Outline platelets.
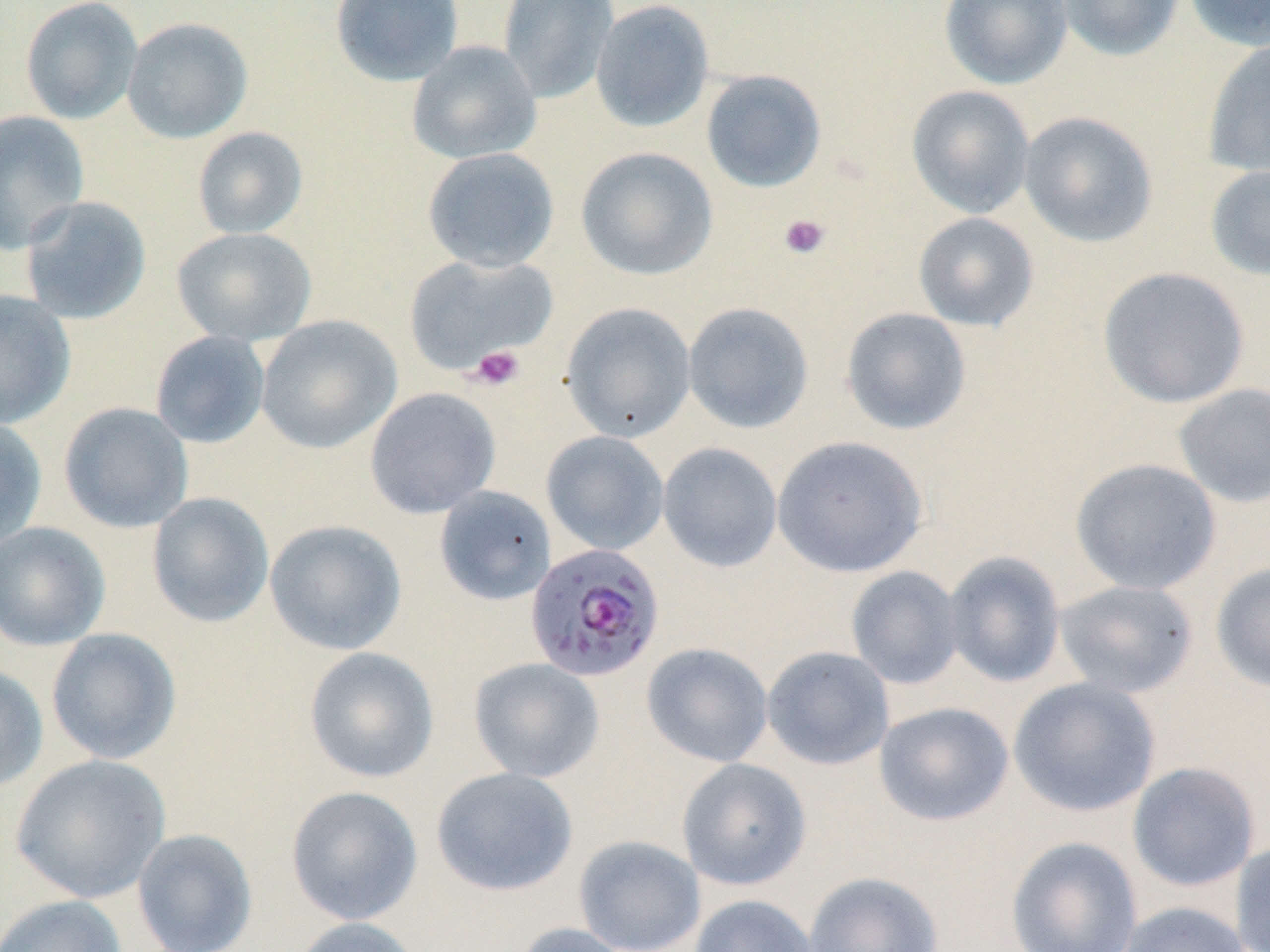

Approximate bounding boxes as named x1/y1/x2/y2 corners in pixels.
Platelets: (x1=778, y1=213, x2=830, y2=260), (x1=469, y1=345, x2=525, y2=391).

slide-level diagnosis = Plasmodium falciparum
stain = May-Grünwald-Giemsa
Plasmodium falciparum-infected red blood cell locations = approximate bounding boxes as named x1/y1/x2/y2 corners in pixels: (x1=525, y1=543, x2=664, y2=683)
image size = 1270×952 pixels
modality = light microscopy
uninfected red blood cell locations = approximate bounding boxes as named x1/y1/x2/y2 corners in pixels: (x1=20, y1=0, x2=143, y2=124), (x1=330, y1=0, x2=464, y2=86), (x1=497, y1=0, x2=619, y2=104), (x1=939, y1=0, x2=1072, y2=89), (x1=1055, y1=0, x2=1185, y2=61), (x1=1183, y1=0, x2=1270, y2=51), (x1=590, y1=1, x2=715, y2=132), (x1=121, y1=16, x2=253, y2=144), (x1=1202, y1=39, x2=1270, y2=179), (x1=406, y1=40, x2=542, y2=165), (x1=700, y1=69, x2=828, y2=193), (x1=906, y1=85, x2=1035, y2=219), (x1=0, y1=110, x2=90, y2=255), (x1=1018, y1=111, x2=1158, y2=248), (x1=192, y1=126, x2=308, y2=239), (x1=575, y1=146, x2=718, y2=281), (x1=421, y1=147, x2=560, y2=273), (x1=1204, y1=163, x2=1270, y2=282), (x1=19, y1=196, x2=152, y2=325), (x1=913, y1=212, x2=1039, y2=332), (x1=172, y1=227, x2=317, y2=347), (x1=404, y1=253, x2=557, y2=375), (x1=1097, y1=266, x2=1250, y2=409), (x1=0, y1=290, x2=76, y2=429), (x1=560, y1=302, x2=696, y2=442), (x1=682, y1=302, x2=814, y2=434), (x1=839, y1=306, x2=972, y2=435), (x1=256, y1=315, x2=401, y2=454), (x1=150, y1=331, x2=270, y2=449), (x1=1173, y1=382, x2=1270, y2=508), (x1=365, y1=387, x2=501, y2=518), (x1=58, y1=402, x2=194, y2=533), (x1=0, y1=414, x2=47, y2=551), (x1=541, y1=431, x2=669, y2=555), (x1=772, y1=435, x2=928, y2=577), (x1=658, y1=442, x2=782, y2=572), (x1=1070, y1=457, x2=1223, y2=596), (x1=434, y1=485, x2=557, y2=605), (x1=146, y1=492, x2=274, y2=628), (x1=264, y1=519, x2=407, y2=655), (x1=0, y1=521, x2=111, y2=652), (x1=942, y1=551, x2=1066, y2=688), (x1=1210, y1=561, x2=1270, y2=693), (x1=845, y1=566, x2=964, y2=690), (x1=1054, y1=579, x2=1198, y2=698), (x1=46, y1=627, x2=182, y2=764), (x1=641, y1=642, x2=773, y2=767), (x1=303, y1=646, x2=439, y2=784), (x1=762, y1=646, x2=894, y2=770), (x1=468, y1=657, x2=605, y2=783), (x1=0, y1=663, x2=49, y2=793), (x1=1008, y1=677, x2=1162, y2=817), (x1=874, y1=701, x2=1014, y2=826), (x1=10, y1=754, x2=171, y2=904), (x1=677, y1=757, x2=811, y2=890), (x1=1126, y1=761, x2=1261, y2=892), (x1=430, y1=767, x2=578, y2=896), (x1=285, y1=785, x2=423, y2=925), (x1=131, y1=828, x2=258, y2=952), (x1=573, y1=835, x2=706, y2=952), (x1=1005, y1=836, x2=1143, y2=951), (x1=1231, y1=840, x2=1270, y2=952), (x1=803, y1=871, x2=943, y2=952), (x1=0, y1=894, x2=128, y2=952), (x1=689, y1=894, x2=820, y2=952), (x1=1116, y1=901, x2=1254, y2=952), (x1=287, y1=917, x2=427, y2=952), (x1=511, y1=922, x2=634, y2=952)
field of view = single
magnification = 1000x
preparation = thin blood film